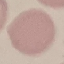
Malaria status: uninfected. Automatically extracted cell patch, resized to 64 × 64 pixels. Giemsa stain. Photographed with a smartphone camera at the microscope eyepiece. Thin blood film.